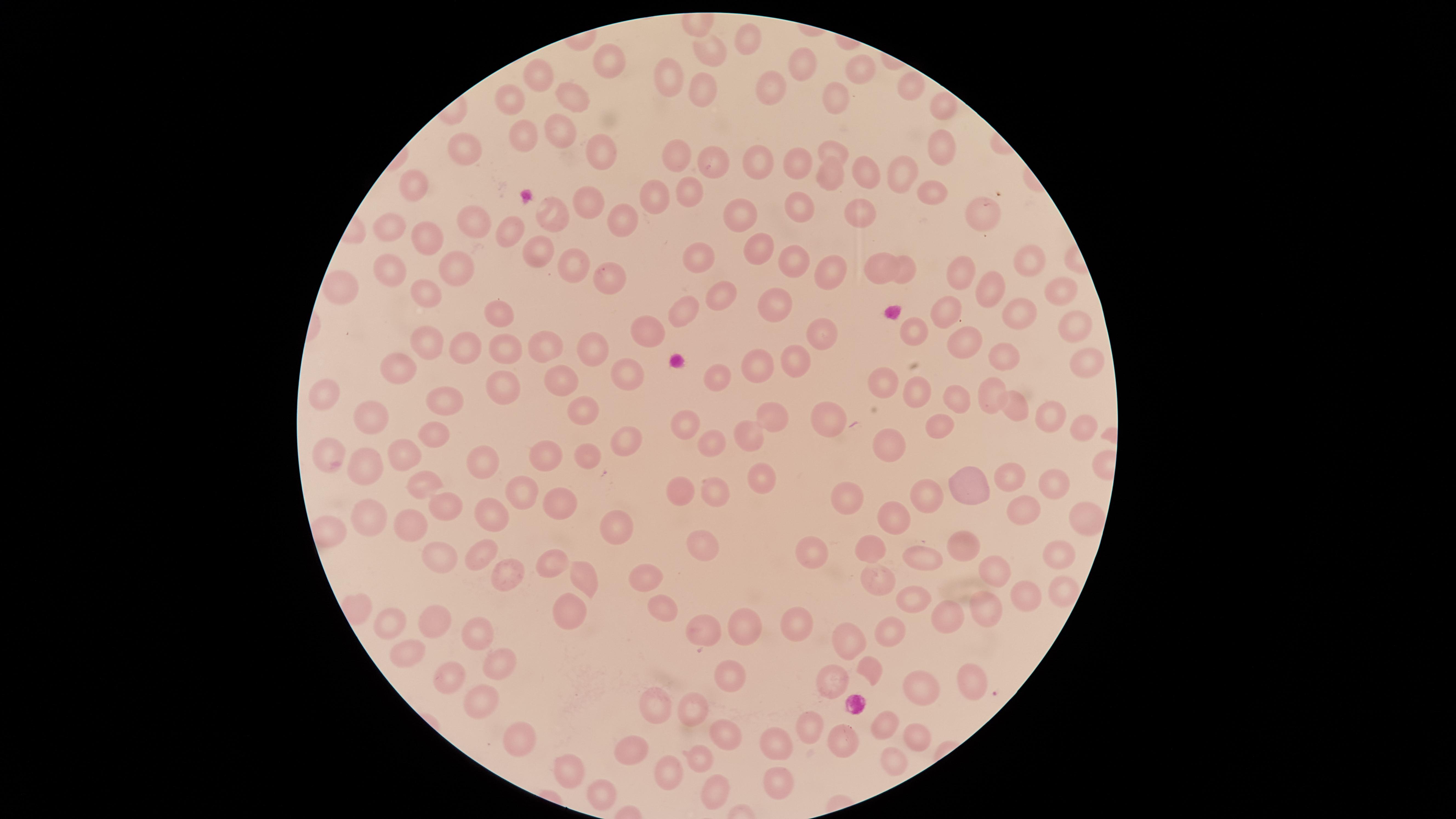
{
  "capture": "smartphone photograph through the microscope eyepiece",
  "image_size": "1456×819 pixels",
  "preparation": "thin blood film",
  "visible_region": "circular",
  "presence": "no malaria parasites detected",
  "stain": "Giemsa",
  "field_of_view": "single",
  "uninfected_RBCs": "approximate marker points as (x, y) in pixels: (745, 38), (711, 53), (608, 57), (809, 66), (858, 66), (543, 76), (671, 76), (774, 87), (908, 91), (574, 92), (704, 93), (514, 99), (838, 99), (942, 106), (554, 130), (520, 136), (471, 144), (595, 151), (835, 151), (941, 151), (674, 155), (716, 162), (799, 162), (756, 164), (862, 175), (902, 178), (831, 179), (418, 185), (691, 190), (655, 192), (927, 193), (590, 201), (798, 211), (858, 214), (552, 215), (979, 216), (743, 217), (620, 218), (475, 225), (396, 227), (509, 230), (427, 235), (762, 248), (532, 253), (791, 261), (699, 262), (1028, 262), (573, 263), (880, 266), (389, 270), (452, 270), (828, 271), (906, 272), (608, 277), (961, 279), (351, 288), (720, 290), (988, 292), (1054, 293), (420, 297), (766, 309), (688, 312), (1018, 312), (490, 313), (949, 313), (1071, 325), (651, 329), (912, 330), (823, 334), (426, 342), (961, 342), (505, 347), (547, 347), (597, 349), (464, 350), (1005, 356), (799, 361), (1087, 362), (402, 367), (757, 367), (623, 372), (717, 374), (559, 379), (504, 381), (887, 381), (991, 390), (331, 391), (916, 395), (446, 399), (956, 400), (1010, 402), (584, 409), (373, 410), (774, 413), (1051, 415), (691, 420), (835, 420), (1084, 425), (616, 430), (750, 430), (941, 430), (434, 432), (712, 438), (893, 444), (592, 450), (543, 452), (406, 455), (330, 457), (483, 462), (366, 465), (762, 477), (1009, 477), (420, 480), (966, 487), (930, 489), (1055, 490), (685, 491), (522, 492), (716, 494), (851, 495), (557, 503), (445, 504), (1025, 507), (890, 515), (370, 517), (490, 518), (1079, 520), (406, 521), (615, 525), (873, 547), (963, 548), (705, 550), (1063, 552), (479, 553), (817, 553), (439, 554), (917, 558), (548, 563), (995, 570), (504, 572), (584, 573), (643, 578), (879, 579), (1057, 595), (1026, 596), (907, 601), (664, 607), (946, 612), (981, 612), (569, 613), (431, 617), (799, 619), (386, 620), (740, 628), (479, 630), (705, 631), (892, 633), (848, 639), (411, 648), (499, 663), (871, 669), (450, 671), (837, 675), (726, 679), (967, 680), (920, 692), (475, 697), (658, 704), (695, 706), (882, 724), (808, 726), (514, 732), (723, 733), (917, 737), (773, 740), (845, 740), (635, 747), (697, 749), (891, 760), (662, 769), (573, 772), (779, 778), (598, 791), (712, 792)"
}